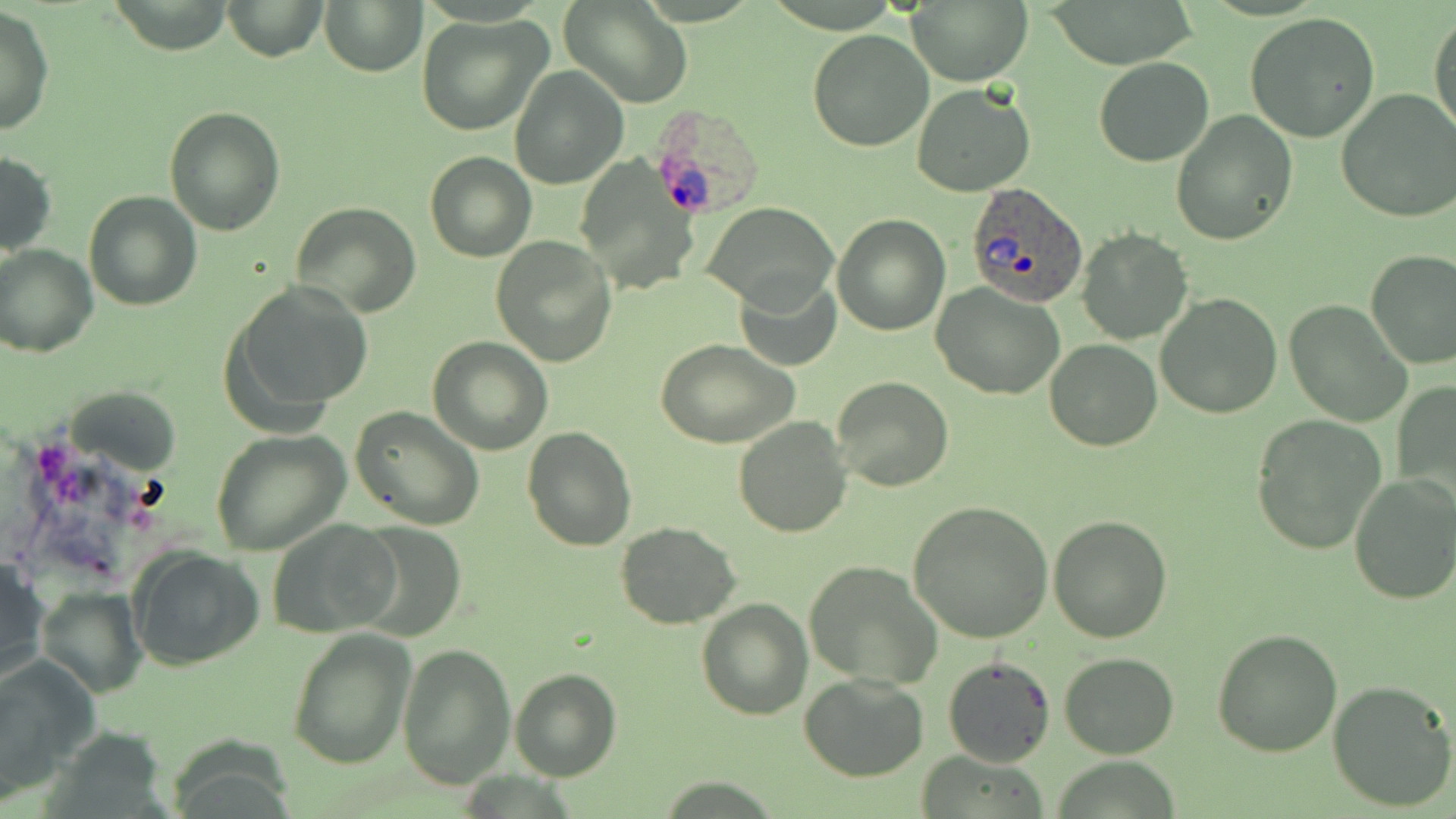
Approximate bounding boxes as named x1/y1/x2/y2 corners in pixels. Uninfected red blood cell locations: (x1=224, y1=0, x2=327, y2=61), (x1=561, y1=0, x2=693, y2=109), (x1=907, y1=0, x2=1032, y2=86), (x1=1041, y1=0, x2=1200, y2=66), (x1=106, y1=1, x2=234, y2=53), (x1=322, y1=2, x2=425, y2=75), (x1=0, y1=7, x2=53, y2=136), (x1=1429, y1=11, x2=1455, y2=140), (x1=1244, y1=12, x2=1381, y2=143), (x1=415, y1=14, x2=551, y2=136), (x1=806, y1=30, x2=933, y2=152), (x1=1093, y1=56, x2=1214, y2=167), (x1=510, y1=65, x2=628, y2=188), (x1=912, y1=85, x2=1036, y2=197), (x1=1336, y1=90, x2=1456, y2=224), (x1=164, y1=105, x2=285, y2=234), (x1=1170, y1=110, x2=1296, y2=246), (x1=424, y1=151, x2=535, y2=262), (x1=0, y1=152, x2=57, y2=256), (x1=83, y1=190, x2=201, y2=311), (x1=704, y1=201, x2=836, y2=308), (x1=292, y1=202, x2=421, y2=317), (x1=832, y1=214, x2=950, y2=335), (x1=1077, y1=229, x2=1191, y2=344), (x1=491, y1=237, x2=617, y2=367), (x1=0, y1=244, x2=97, y2=357), (x1=1365, y1=249, x2=1456, y2=370), (x1=733, y1=273, x2=841, y2=371), (x1=226, y1=279, x2=374, y2=423), (x1=931, y1=284, x2=1064, y2=400), (x1=1156, y1=292, x2=1282, y2=419), (x1=1284, y1=299, x2=1413, y2=427), (x1=429, y1=337, x2=551, y2=455), (x1=656, y1=339, x2=799, y2=449), (x1=1044, y1=340, x2=1162, y2=451), (x1=831, y1=376, x2=954, y2=492), (x1=1393, y1=379, x2=1456, y2=504), (x1=68, y1=386, x2=180, y2=471), (x1=350, y1=407, x2=485, y2=532), (x1=1250, y1=415, x2=1387, y2=555), (x1=732, y1=417, x2=852, y2=538), (x1=521, y1=426, x2=635, y2=550), (x1=211, y1=430, x2=349, y2=555), (x1=1348, y1=475, x2=1456, y2=606), (x1=906, y1=501, x2=1053, y2=643), (x1=1048, y1=515, x2=1175, y2=643), (x1=270, y1=519, x2=401, y2=637), (x1=351, y1=521, x2=464, y2=639), (x1=615, y1=522, x2=740, y2=629), (x1=129, y1=547, x2=264, y2=671), (x1=0, y1=558, x2=50, y2=689), (x1=803, y1=561, x2=942, y2=688), (x1=38, y1=587, x2=148, y2=699), (x1=696, y1=598, x2=813, y2=720), (x1=287, y1=627, x2=416, y2=771), (x1=1212, y1=628, x2=1344, y2=756), (x1=398, y1=644, x2=514, y2=787), (x1=1060, y1=653, x2=1180, y2=759), (x1=0, y1=654, x2=98, y2=797), (x1=942, y1=655, x2=1055, y2=768), (x1=509, y1=668, x2=623, y2=781), (x1=799, y1=673, x2=929, y2=781), (x1=1327, y1=679, x2=1455, y2=812). Plasmodium ovale-infected red blood cell locations: (x1=653, y1=104, x2=757, y2=221), (x1=965, y1=182, x2=1090, y2=306). Slide-level diagnosis: Plasmodium ovale. Thin blood film. 1000x magnification. Light microscopy. One field of a larger specimen. Image is 1456×819 pixels. May-Grünwald-Giemsa stain.